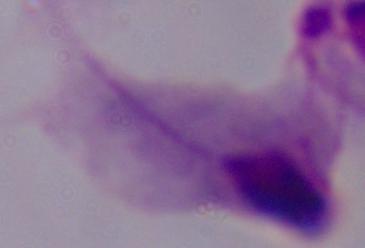

Micrograph. A trichomonad is shown. Captured at 1000x magnification.